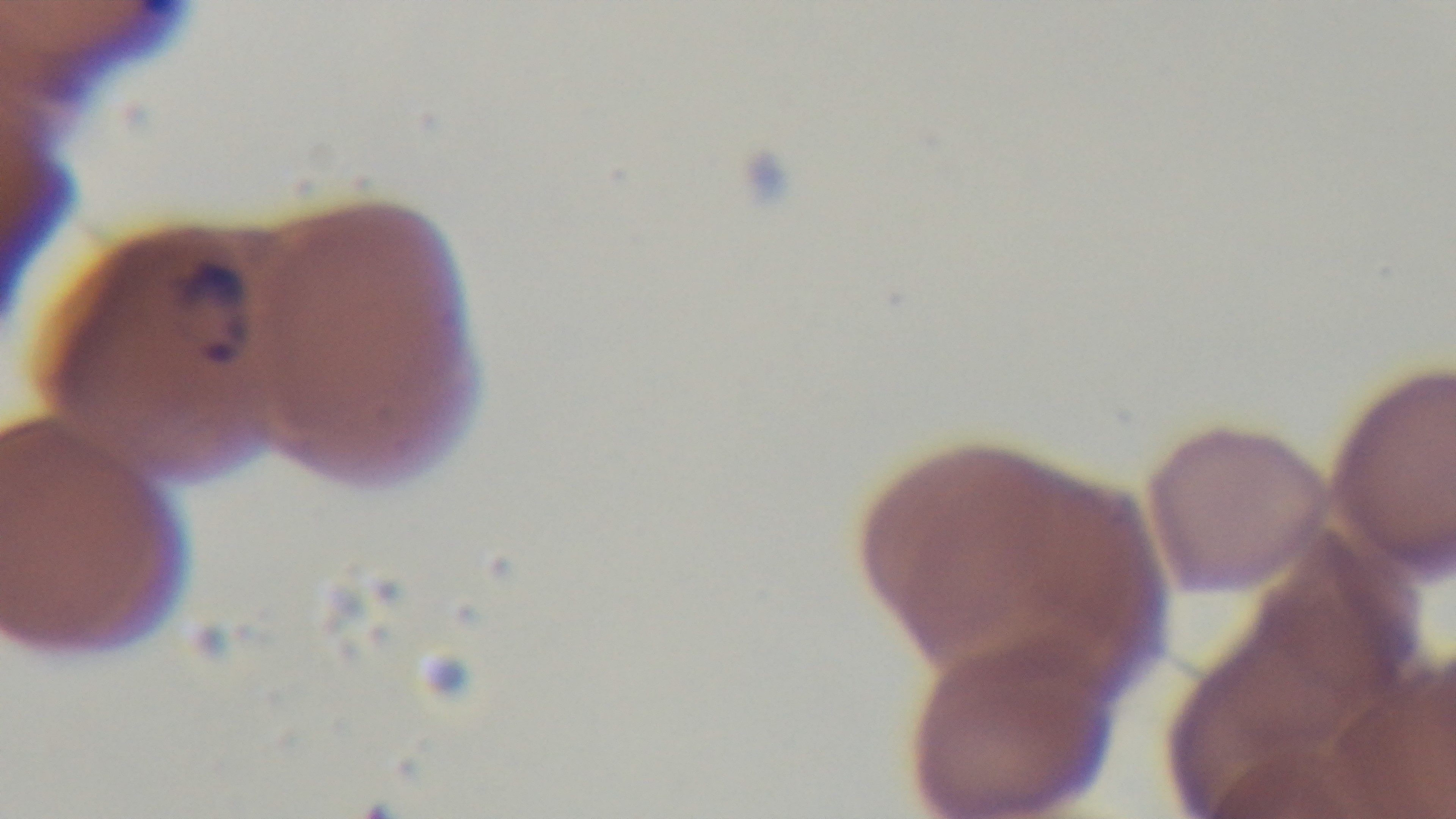

Summary:
  - Objective: 100x oil immersion
  - Preparation: thin
  - Modality: light microscopy
  - Capture: mounted 4K digital camera
  - Malaria status: infected
  - Stain: Giemsa
  - Field of view: one from the slide